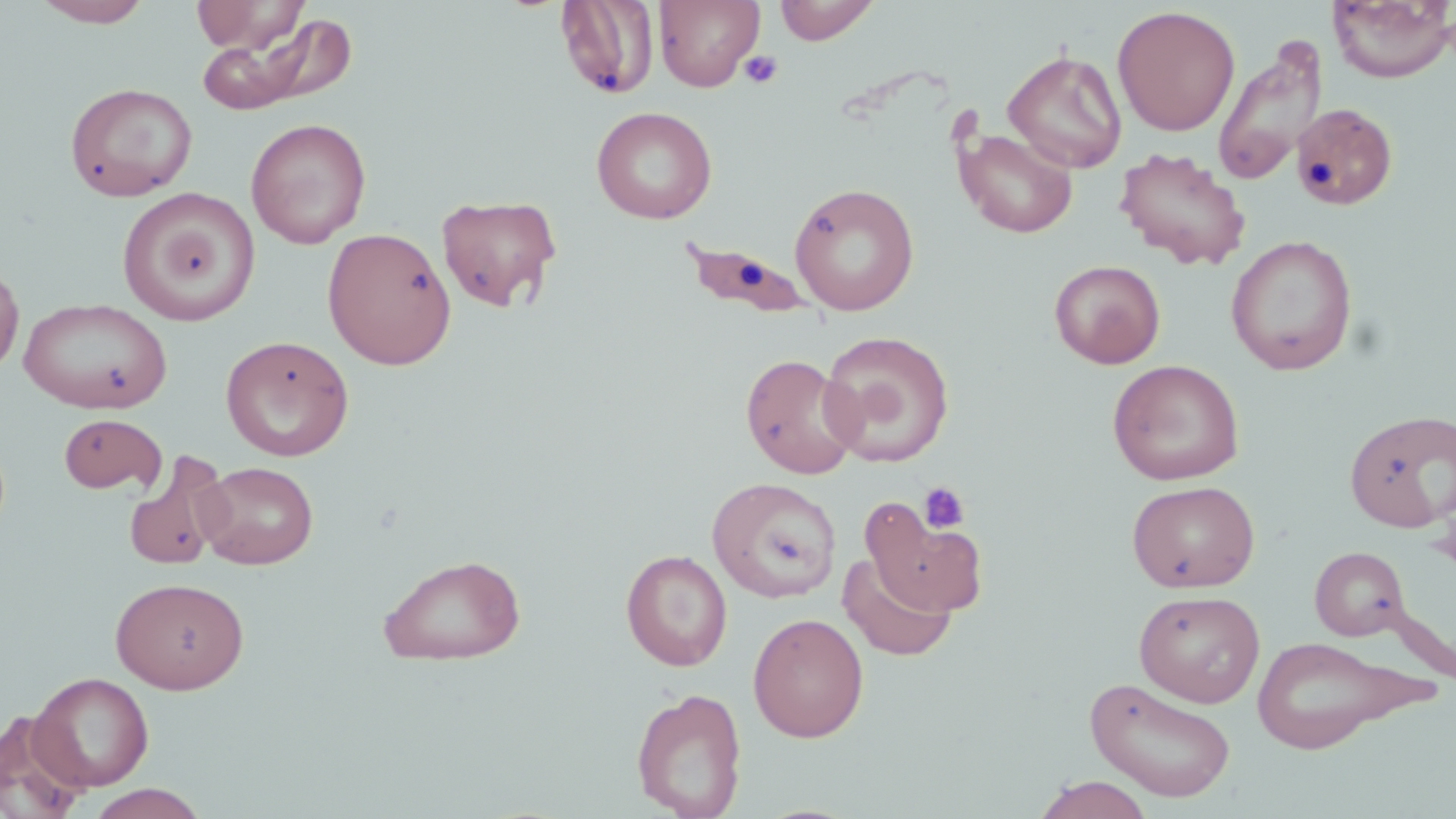
Approximate bounding boxes as (x1,y1)-(x2,y2) corner pairs in pixels. Platelet locations: (739,50)-(783,89), (918,481)-(971,535). Uninfected red blood cell locations: (32,0)-(154,27), (190,0)-(308,54), (654,0)-(764,92), (774,0)-(880,44), (555,1)-(660,100), (1327,1)-(1454,84), (1112,5)-(1240,137), (208,13)-(359,113), (1212,37)-(1328,187), (1003,49)-(1127,173), (65,82)-(197,201), (1291,101)-(1399,212), (591,106)-(717,224), (245,117)-(371,249), (956,128)-(1078,238), (1115,147)-(1251,271), (789,182)-(920,316), (117,187)-(259,327), (437,194)-(563,313), (676,224)-(824,325), (322,226)-(457,369), (1225,234)-(1358,376), (1048,259)-(1166,369), (0,263)-(24,379), (19,297)-(172,414), (819,330)-(955,467), (220,334)-(354,461), (740,353)-(861,480), (1108,359)-(1245,485), (1344,409)-(1456,533), (58,413)-(167,494), (123,451)-(233,571), (197,461)-(318,569), (706,477)-(842,602), (1127,480)-(1260,593), (864,500)-(986,617), (1310,546)-(1411,641), (621,549)-(733,670), (377,553)-(527,666), (838,553)-(957,661), (110,577)-(249,693), (1134,590)-(1265,707), (748,613)-(869,742), (1250,635)-(1407,753), (29,671)-(154,791), (1084,676)-(1237,802), (631,686)-(748,819), (0,711)-(91,819), (1033,775)-(1154,819), (83,784)-(210,819). Slide-level diagnosis: negative for blood parasites. Light microscopy. 1000x magnification. Image is 1456×819 pixels. Thin blood film. Single field of view. May-Grünwald-Giemsa-stained preparation.